Report the malaria status of this cell.
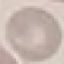

Uninfected.

capture = smartphone camera at the microscope eyepiece
stain = Giemsa
preparation = thin smear
image type = cell patch, automatically extracted from a larger field of view and resized to 64 × 64 pixels